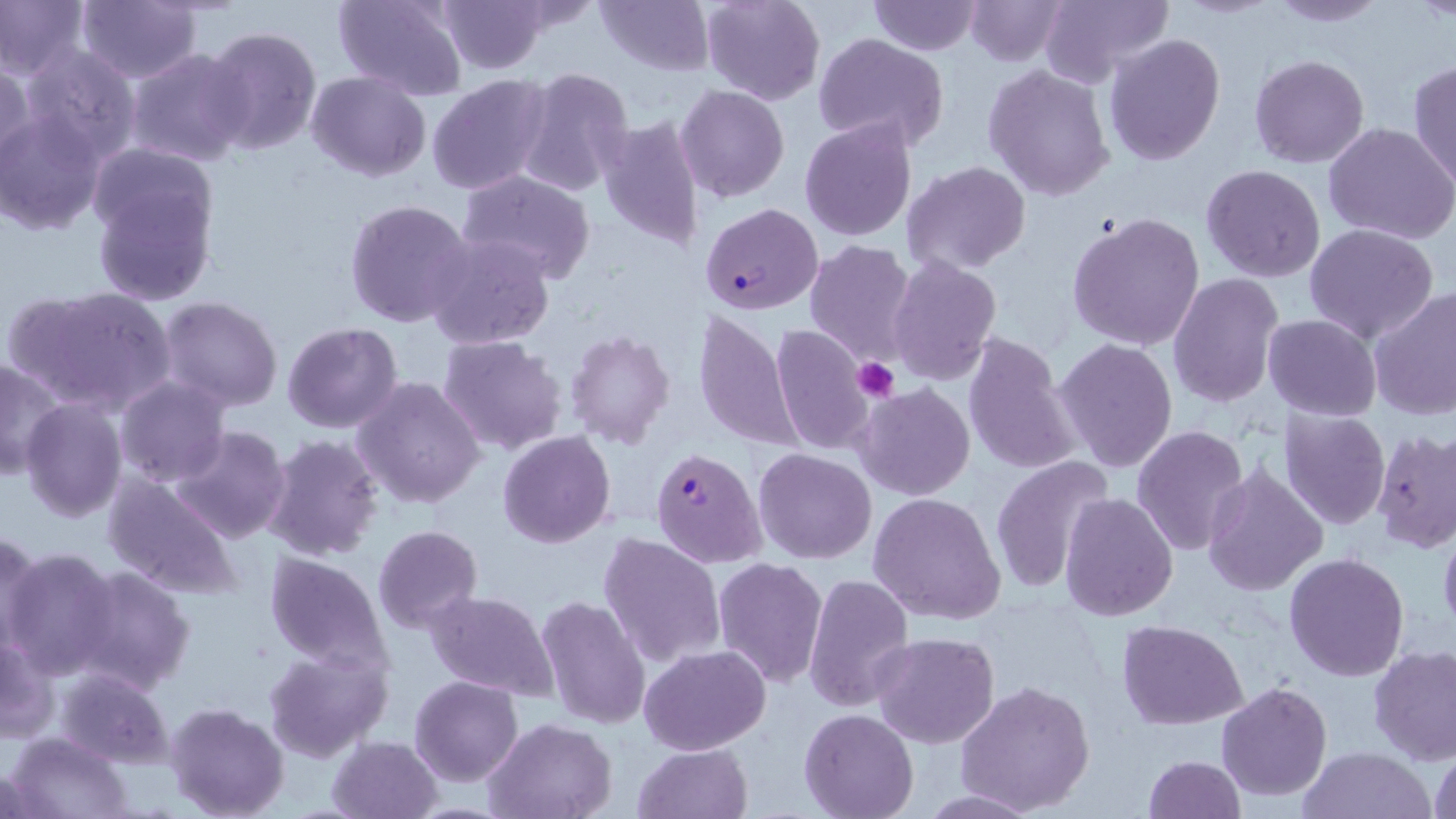

Summary:
  - Coordinate format: approximate bounding boxes as (x1, y1, x2, y2) in pixels
  - Platelet locations: (852, 357, 901, 403)
  - Uninfected red blood cell locations: (74, 0, 203, 83), (334, 0, 469, 100), (436, 0, 548, 74), (593, 0, 713, 76), (699, 0, 825, 106), (867, 0, 984, 55), (965, 0, 1069, 66), (1038, 0, 1173, 89), (0, 1, 87, 80), (1266, 1, 1388, 26), (203, 26, 321, 155), (813, 33, 948, 151), (1103, 34, 1227, 165), (20, 43, 141, 160), (127, 49, 253, 166), (1248, 55, 1369, 169), (0, 61, 35, 172), (1408, 62, 1455, 187), (982, 63, 1115, 201), (514, 67, 634, 195), (306, 71, 432, 182), (427, 73, 555, 196), (676, 83, 789, 203), (0, 110, 107, 235), (597, 112, 705, 255), (800, 118, 919, 240), (1323, 122, 1456, 244), (87, 143, 216, 246), (903, 161, 1030, 273), (1201, 164, 1326, 282), (459, 170, 596, 282), (91, 182, 216, 305), (344, 198, 475, 329), (1065, 210, 1207, 352), (1303, 224, 1441, 347), (423, 231, 556, 351), (804, 239, 917, 364), (886, 255, 1002, 385), (1169, 274, 1285, 409), (11, 285, 178, 415), (1369, 287, 1456, 421), (159, 295, 284, 413), (693, 306, 801, 453), (1263, 314, 1381, 420), (281, 321, 404, 433), (769, 324, 874, 456), (566, 329, 676, 448), (963, 331, 1080, 476), (437, 335, 568, 457), (309, 337, 445, 485), (1052, 337, 1178, 473), (0, 356, 67, 484), (354, 374, 487, 508), (116, 376, 231, 489), (855, 383, 977, 500), (18, 397, 129, 521), (1279, 407, 1389, 530), (1131, 425, 1250, 555), (168, 426, 292, 546), (497, 430, 616, 548), (1371, 430, 1456, 555), (261, 433, 385, 561), (754, 448, 875, 565), (990, 457, 1115, 595), (1200, 466, 1328, 597), (103, 474, 243, 600), (867, 492, 1006, 626), (1061, 493, 1179, 622), (1438, 517, 1456, 637), (373, 524, 482, 632), (1, 532, 45, 656), (598, 533, 725, 667), (2, 547, 121, 678), (264, 551, 393, 676), (1283, 552, 1410, 682), (712, 557, 829, 687), (70, 564, 195, 696), (802, 574, 914, 712), (424, 589, 560, 702), (536, 594, 651, 729), (1117, 619, 1246, 729), (1, 632, 57, 744), (871, 632, 1000, 748), (639, 644, 770, 755), (265, 646, 391, 760), (1369, 646, 1456, 767), (56, 668, 175, 766), (410, 675, 524, 784), (956, 680, 1097, 815), (1216, 681, 1332, 801), (165, 702, 290, 819), (798, 709, 920, 819), (485, 717, 619, 819), (6, 733, 134, 819), (328, 735, 443, 819), (1429, 742, 1456, 819), (633, 743, 751, 819), (1301, 747, 1433, 819), (1143, 755, 1245, 818)
  - Plasmodium falciparum-infected red blood cell locations: (700, 202, 822, 315), (651, 448, 766, 568)
  - Slide-level diagnosis: Plasmodium falciparum
  - Magnification: 1000x
  - Field of view: one of a larger specimen
  - Preparation: thin blood film
  - Stain: May-Grünwald-Giemsa
  - Image size: 1456×819 pixels
  - Modality: optical microscopy